Comment on the morphology of the erythrocytes.
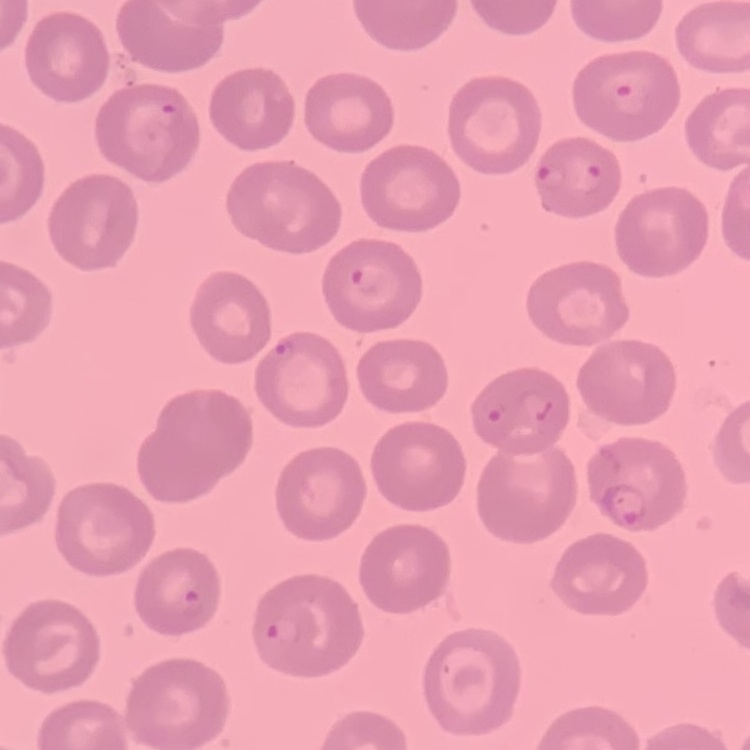

No rouleaux formation.

One tile cut from a larger photomicrograph. Field's or Giemsa stain. Thin peripheral smear.